Identify the parasite.
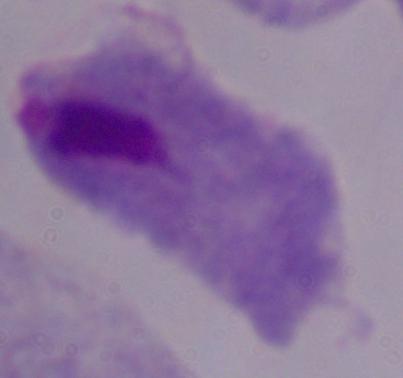
This is a trichomonad.

Summary:
  - Modality: photomicrograph
  - Magnification: 1000x